Comment on the morphology of the erythrocytes.
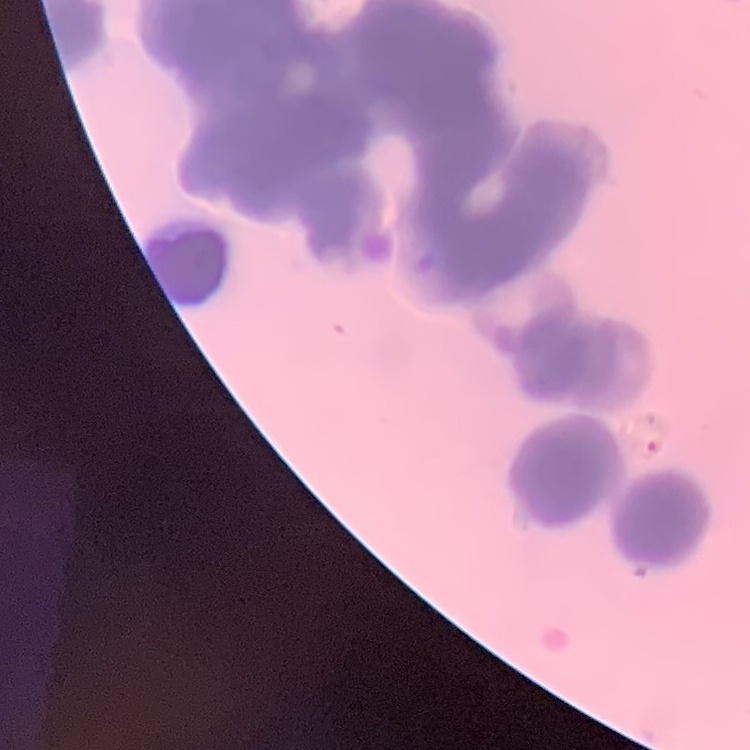

They show rouleaux formation.

Summary:
  - Preparation: thin peripheral smear
  - Image type: one tile cut from a larger photomicrograph
  - Stain: Field's or Giemsa